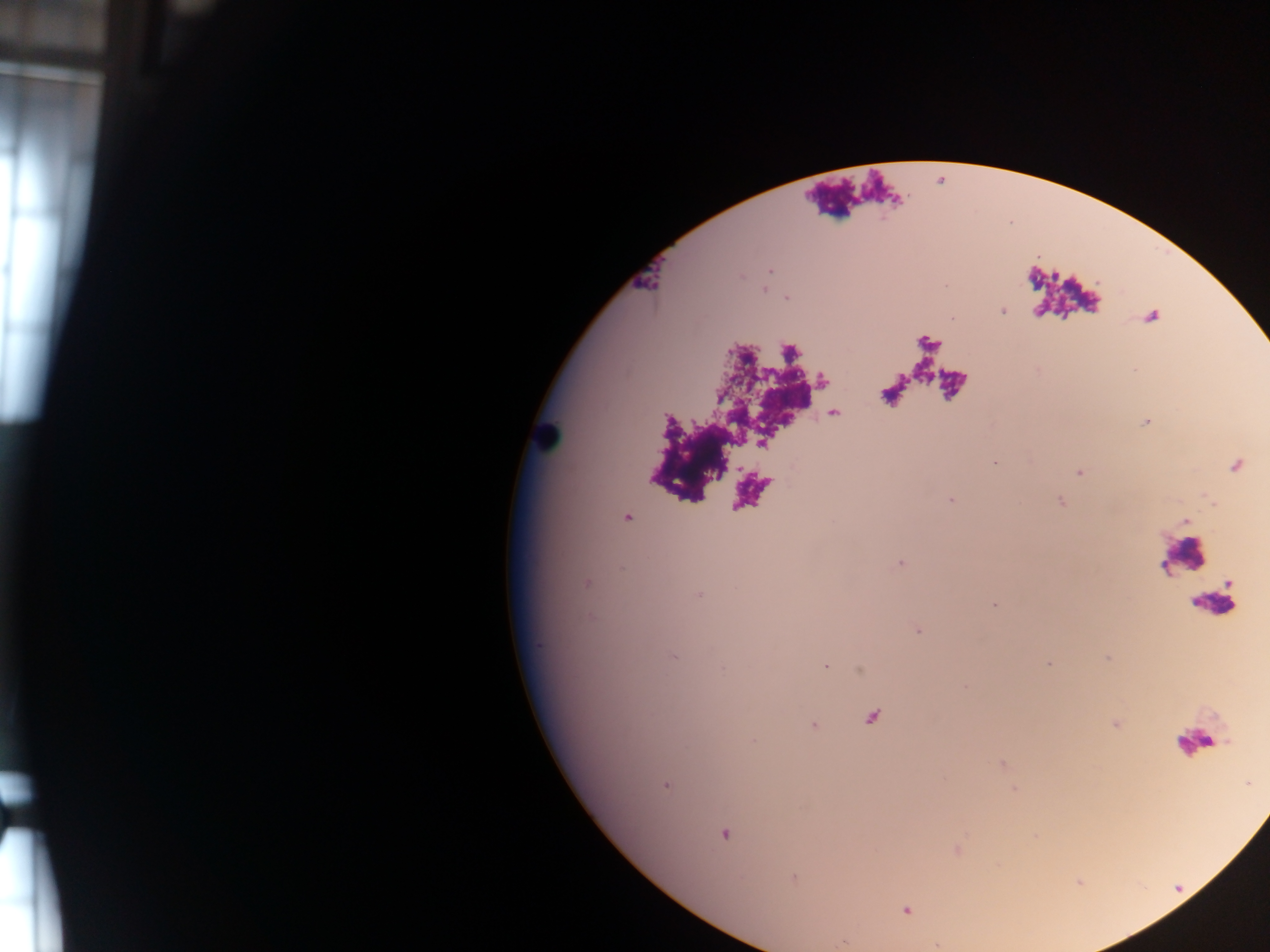
Approximate centers as x y in pixels.
Summary:
  - Leukocyte locations: 547 433; 1183 558
  - Malaria parasite locations: 770 270; 786 298; 1003 311; 994 462; 950 500; 627 517; 900 563; 587 584; 698 594; 994 605; 918 632; 673 656; 1048 664; 825 666; 723 668; 814 725; 754 740; 666 785; 724 834; 794 878; 906 910
  - Country: Ghana
  - Preparation: thick blood film
  - Capture: mobile-phone photograph through a microscope
  - Field of view: single
  - Image size: 1270×952 pixels